Report the malaria status of this cell.
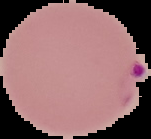
It is parasitized.

Summary:
  - Image size: 151×139 pixels
  - Image type: segmented cell region on a black background
  - Preparation: thin blood film